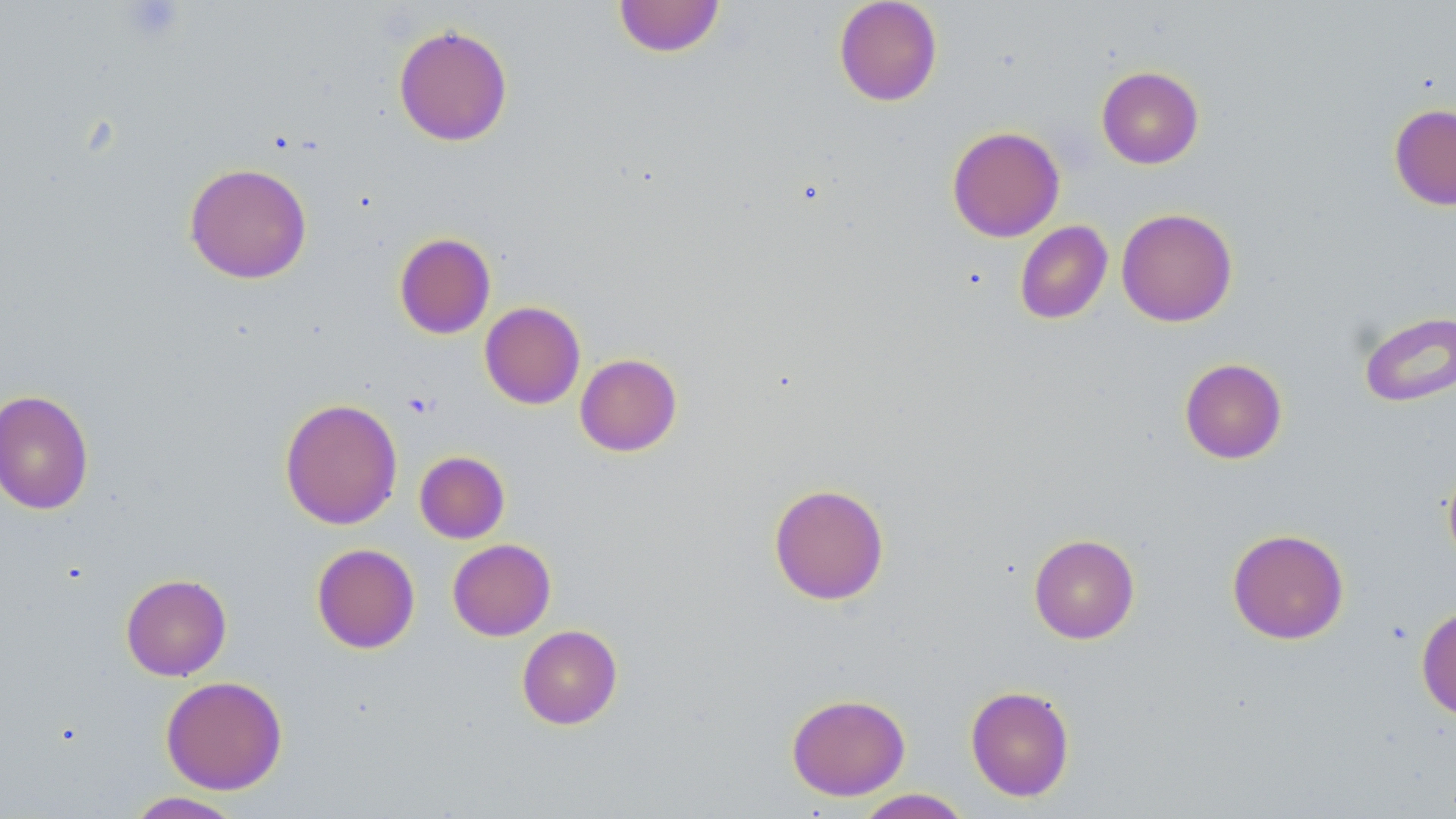
Summary:
  - Coordinate format: approximate bounding boxes as (x1,y1)-(x2,y2) corner pairs in pixels
  - Uninfected red blood cell locations: (613,0)-(726,58), (833,0)-(943,107), (393,23)-(513,146), (1096,66)-(1204,169), (1389,104)-(1456,211), (947,126)-(1065,242), (184,163)-(312,284), (1116,208)-(1238,327), (1014,220)-(1113,325), (394,232)-(496,339), (479,301)-(586,409), (1358,310)-(1456,407), (574,353)-(683,456), (1179,358)-(1287,464), (0,389)-(95,515), (279,397)-(403,530), (414,451)-(510,543), (1442,460)-(1456,574), (768,483)-(889,605), (1226,528)-(1349,644), (1028,533)-(1140,644), (447,539)-(556,641), (311,543)-(420,654), (121,573)-(232,681), (1416,605)-(1456,722), (516,624)-(623,729), (160,675)-(288,795), (965,685)-(1075,802), (786,693)-(911,800), (854,789)-(972,818), (125,791)-(245,818)
  - Platelet locations: (123,1)-(185,42)
  - Slide-level diagnosis: negative for blood parasites
  - Stain: May-Grünwald-Giemsa
  - Preparation: thin blood film
  - Modality: optical microscopy
  - Field of view: single
  - Magnification: 1000x
  - Image size: 1456×819 pixels